Name the blood parasite species.
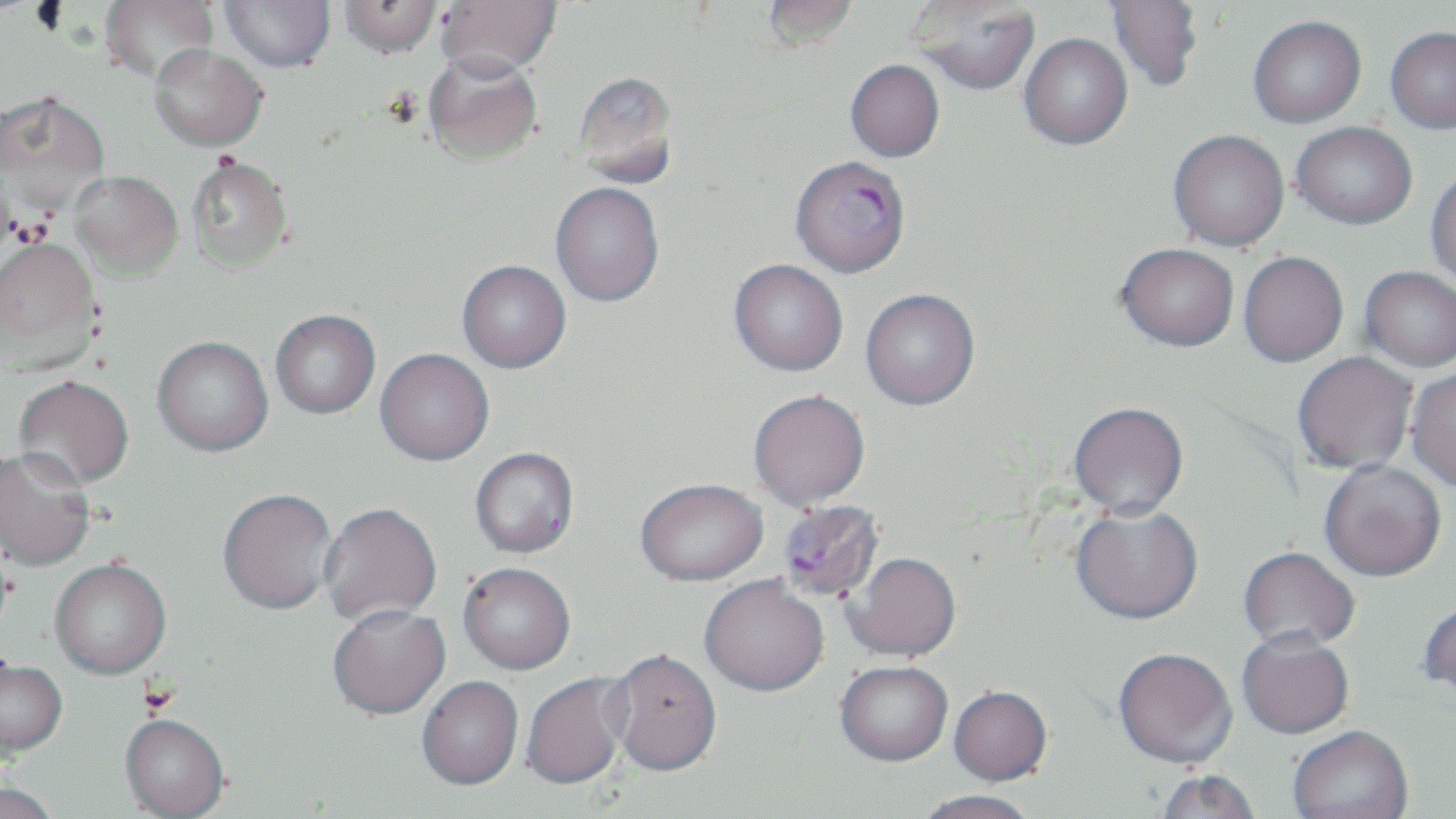

Plasmodium falciparum.

Approximate bounding boxes as (x1, y1, x2, y2) in pixels. Uninfected red blood cell locations: (99, 0, 219, 84), (220, 0, 335, 72), (339, 0, 442, 58), (435, 0, 562, 78), (762, 0, 860, 52), (912, 0, 1041, 95), (1106, 0, 1203, 91), (1248, 15, 1366, 127), (1385, 25, 1456, 133), (1020, 33, 1132, 149), (150, 44, 267, 151), (422, 51, 542, 166), (845, 59, 944, 162), (572, 70, 679, 187), (0, 91, 110, 214), (1292, 121, 1417, 229), (1168, 129, 1289, 251), (186, 154, 294, 274), (71, 170, 183, 280), (1426, 170, 1456, 289), (551, 181, 664, 307), (0, 236, 102, 369), (1116, 243, 1239, 352), (1239, 251, 1348, 366), (729, 259, 848, 377), (457, 260, 571, 373), (1360, 266, 1456, 372), (860, 288, 980, 412), (270, 310, 381, 420), (152, 336, 274, 458), (374, 350, 494, 468), (1292, 353, 1418, 475), (1406, 368, 1456, 493), (13, 375, 134, 491), (749, 391, 871, 512), (1068, 404, 1188, 522), (0, 448, 95, 572), (471, 448, 579, 560), (1319, 461, 1446, 584), (636, 482, 769, 588), (218, 491, 338, 618), (319, 505, 442, 627), (1071, 507, 1204, 628), (1238, 548, 1359, 654), (844, 555, 961, 664), (50, 562, 171, 682), (458, 565, 575, 676), (699, 578, 829, 699), (1418, 602, 1456, 705), (328, 607, 451, 723), (1237, 635, 1354, 741), (608, 651, 723, 780), (1113, 651, 1238, 771), (0, 662, 68, 763), (835, 664, 952, 769), (521, 673, 630, 793), (417, 677, 523, 792), (948, 688, 1052, 788), (119, 717, 229, 819), (1288, 728, 1413, 819), (1153, 772, 1260, 819), (0, 783, 61, 819), (913, 792, 1041, 819). Plasmodium falciparum-infected red blood cell locations: (790, 154, 911, 278), (783, 501, 894, 601). One field of a larger specimen. Captured at 1000x magnification. Optical microscopy. May-Grünwald-Giemsa stain. Image is 1456×819 pixels. Thin blood smear.